Assess this cell for malaria.
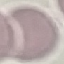

It is uninfected.

Summary:
  - Preparation: thin blood film
  - Image type: cell patch, automatically extracted from a larger field of view and resized to 64 × 64 pixels
  - Stain: Giemsa
  - Capture: smartphone through the microscope eyepiece